Assess this cell for malaria.
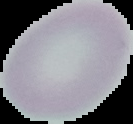

Uninfected.

Summary:
  - Preparation: thin blood film
  - Image type: segmented cell region with the area outside set to black
  - Image size: 133×124 pixels